Report the malaria status of this cell.
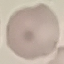

It is uninfected.

stain = Giemsa
capture = smartphone through the microscope eyepiece
preparation = thin blood smear
image type = automatically extracted cell patch, resized to 64 × 64 pixels